Locate malaria parasites and identify their life-cycle stages.
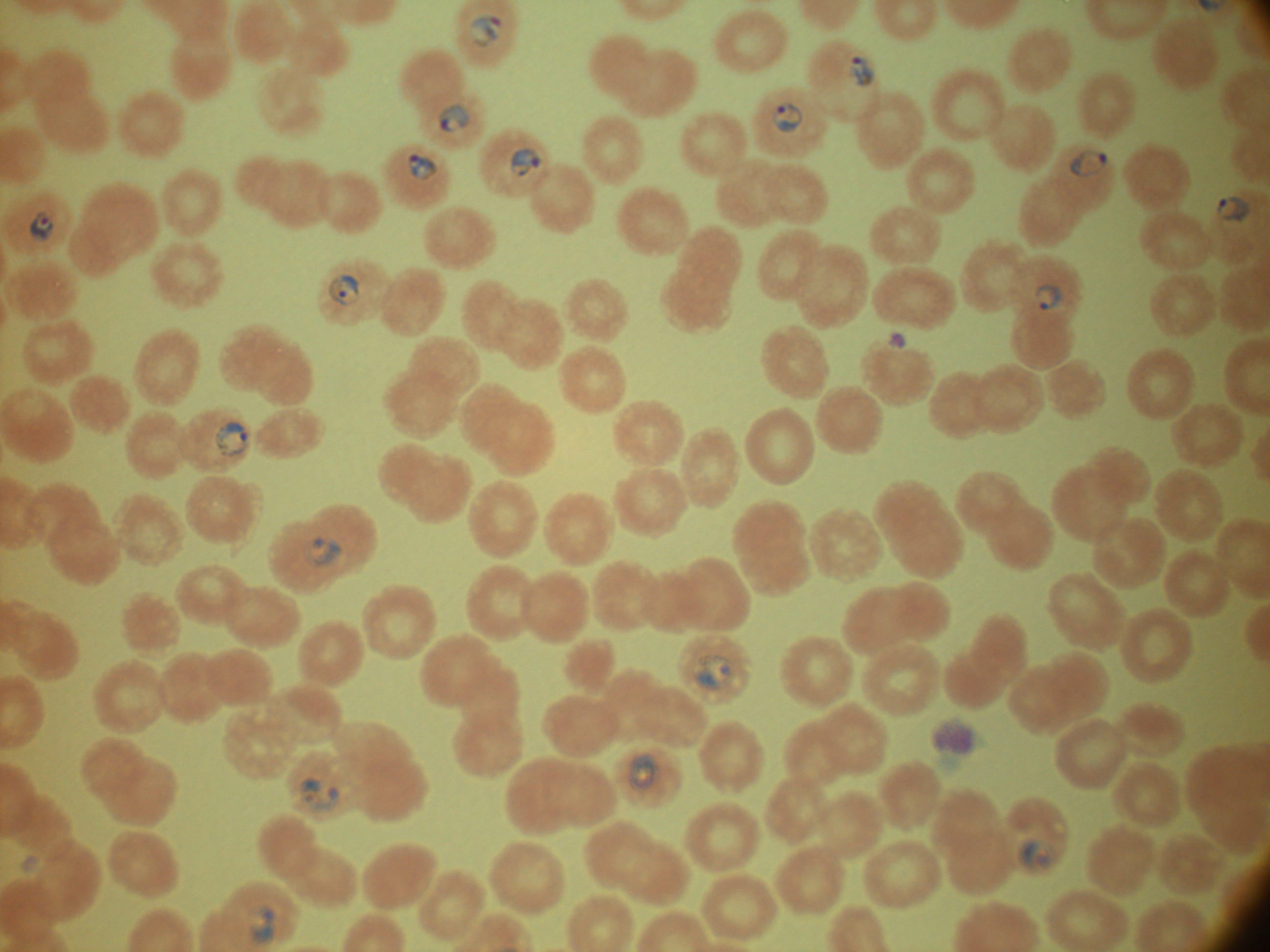

Approximate bounding boxes as (x1, y1, x2, y2) in pixels, from the source annotation, which is not necessarily exhaustive.
Ring forms: (469, 16, 503, 47), (850, 56, 876, 87), (438, 103, 468, 134), (772, 103, 804, 132), (511, 147, 540, 177), (1070, 150, 1108, 177), (408, 153, 438, 181), (1217, 196, 1252, 221), (30, 211, 54, 241), (329, 273, 360, 305), (1036, 283, 1063, 309), (216, 422, 246, 456), (304, 535, 342, 568), (693, 655, 736, 689), (627, 755, 656, 791), (300, 778, 340, 811), (1018, 840, 1055, 874), (251, 904, 275, 942).

Thin blood smear. Image is 1270×952 pixels. Captured at 100x magnification. Species: Plasmodium falciparum. One field from this slide. Giemsa-stained preparation. Leica DM2000 optical microscope with a built-in camera.